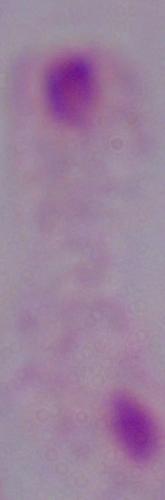

Summary:
  - Magnification: 1000x
  - Identification: trichomonad
  - Modality: photomicrograph